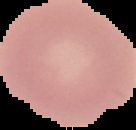
Summary:
  - Malaria status: uninfected
  - Image size: 136×130 pixels
  - Image type: segmented cell region with the area outside set to black
  - Preparation: thin blood smear